State which parasite is depicted.
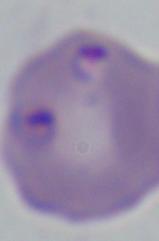
Babesia.

{
  "magnification": "1000x",
  "modality": "micrograph"
}